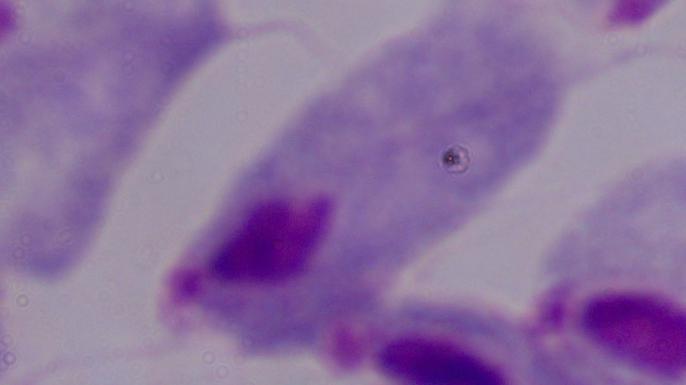

magnification = 1000x
identification = trichomonad
modality = photomicrograph